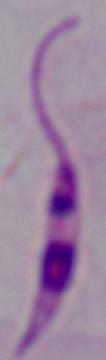
Summary:
  - Magnification: 1000x
  - Modality: micrograph
  - Identification: Leishmania